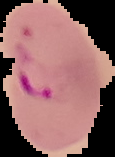
Summary:
  - Image size: 115×157 pixels
  - Preparation: thin blood film
  - Image type: segmented cell region on a black background
  - Result: malaria parasites identified